Give the position of every Plasmodium parasite visible.
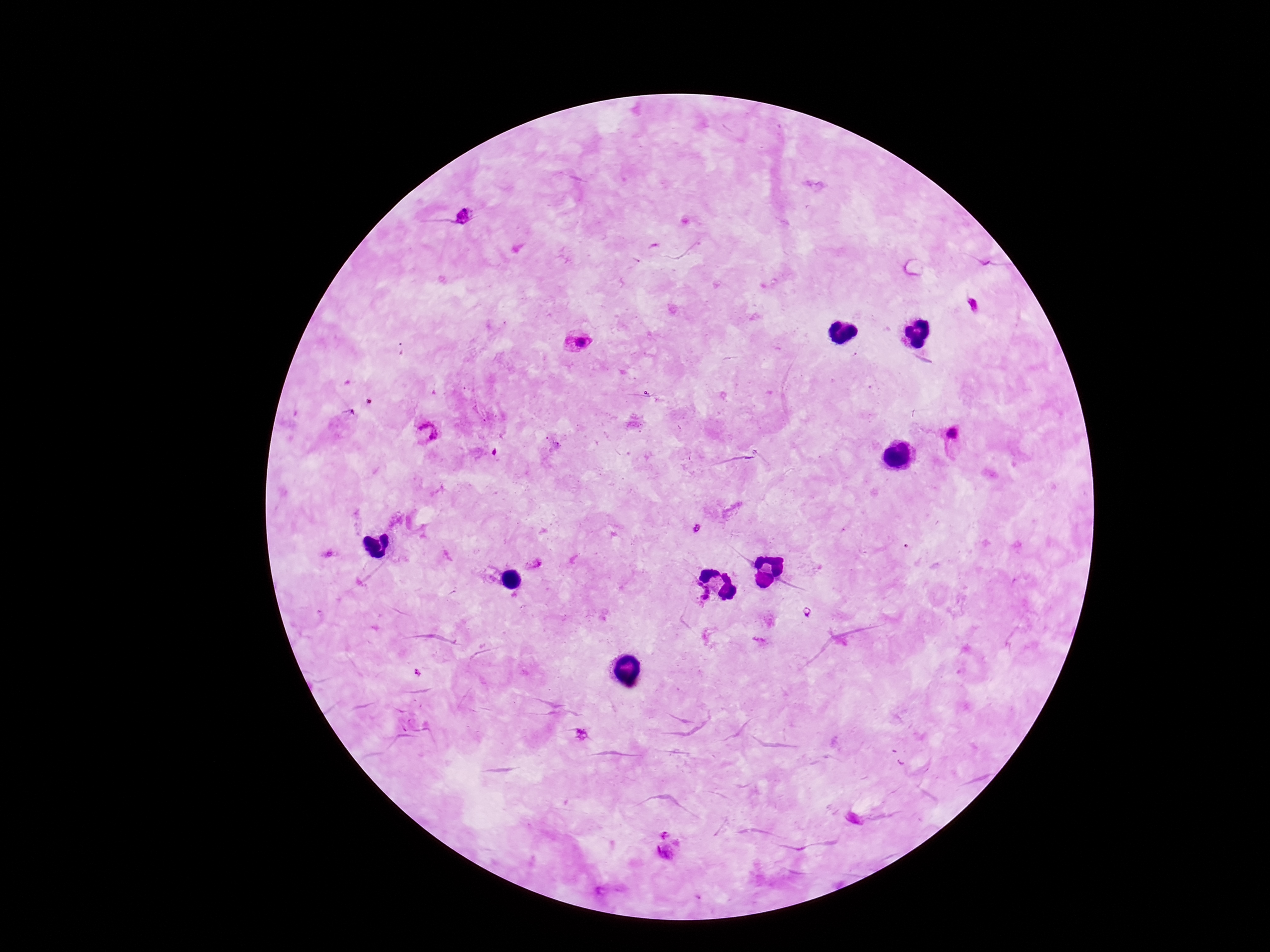
Approximate object centers, in pixels from the top-left corner.
Plasmodium parasites: (x=465, y=216), (x=972, y=305), (x=576, y=341), (x=426, y=434), (x=952, y=434), (x=535, y=564), (x=696, y=592), (x=418, y=673), (x=581, y=734), (x=666, y=833), (x=666, y=853).

Summary:
  - Preparation: thick blood film
  - Stain: Giemsa
  - Magnification: 100x
  - Image size: 1270×952 pixels
  - Field of view: one from this slide
  - Patient malaria status: positive
  - Capture: smartphone camera through the microscope eyepiece